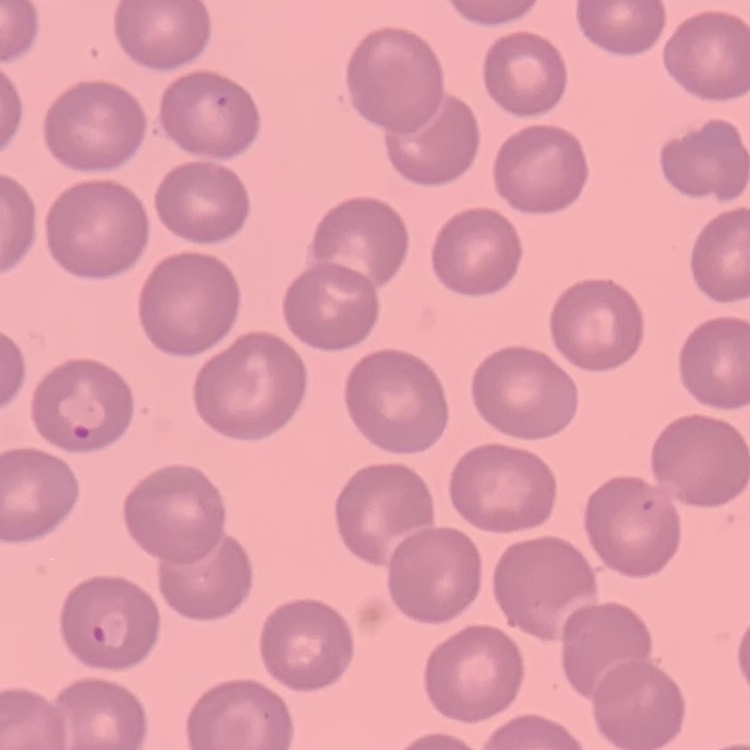
Summary:
  - Red blood cell morphology: no rouleaux formation
  - Stain: Field's or Giemsa
  - Image type: square crop of a larger photomicrograph
  - Preparation: thin peripheral smear